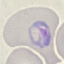 Malaria status: parasitized. Giemsa-stained preparation. Thin blood film. Cell patch, automatically extracted from a larger field of view and resized to 64 × 64 pixels. Acquired by smartphone through the microscope eyepiece.